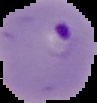

{
  "preparation": "thin blood smear",
  "image_size": "97×103 pixels",
  "malaria_status": "parasitized",
  "image_type": "segmented cell region with the area outside set to black"
}